Outline each uninfected red blood cell.
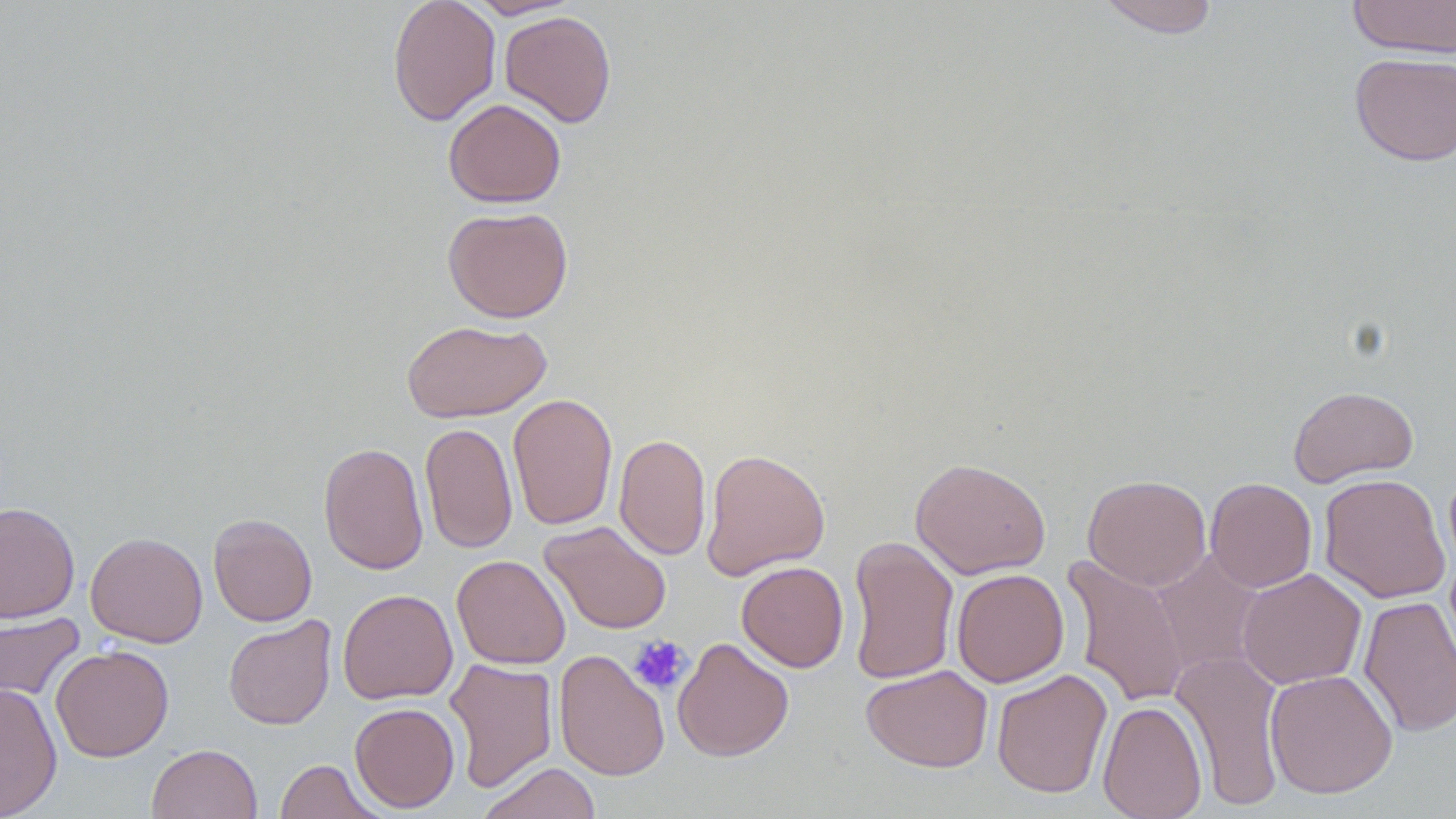
Approximate bounding boxes as (x1,y1)-(x2,y2) corner pairs in pixels.
Uninfected red blood cells: (387,0)-(501,126), (465,0)-(581,19), (1096,0)-(1220,38), (1346,0)-(1456,58), (499,10)-(617,128), (1350,52)-(1455,166), (443,98)-(566,207), (442,206)-(574,323), (402,319)-(552,423), (1287,385)-(1419,487), (507,393)-(618,531), (420,422)-(518,554), (614,432)-(712,561), (318,442)-(429,575), (701,448)-(830,580), (910,457)-(1051,579), (1319,473)-(1450,603), (1083,474)-(1211,591), (1205,477)-(1317,592), (0,502)-(80,622), (208,513)-(317,626), (539,520)-(672,635), (85,531)-(208,648), (846,535)-(959,685), (1150,550)-(1265,679), (452,554)-(570,669), (1062,554)-(1191,708), (736,561)-(849,672), (951,568)-(1069,687), (1237,568)-(1366,689), (338,588)-(458,705), (1358,595)-(1456,737), (0,611)-(85,707), (223,615)-(337,730), (672,637)-(794,762), (50,645)-(174,762), (554,649)-(670,781), (1170,649)-(1287,810), (444,657)-(558,793), (861,664)-(993,772), (991,668)-(1112,798), (1264,669)-(1398,799), (0,682)-(62,818), (1097,699)-(1207,819), (350,702)-(460,812), (146,743)-(263,819), (275,758)-(384,819), (477,762)-(602,819).

Summary:
  - Platelet locations: (629,635)-(692,694)
  - Slide-level diagnosis: no evidence of blood parasites
  - Modality: light microscopy
  - Preparation: thin blood film
  - Stain: May-Grünwald-Giemsa
  - Image size: 1456×819 pixels
  - Magnification: 1000x
  - Field of view: one of a larger specimen